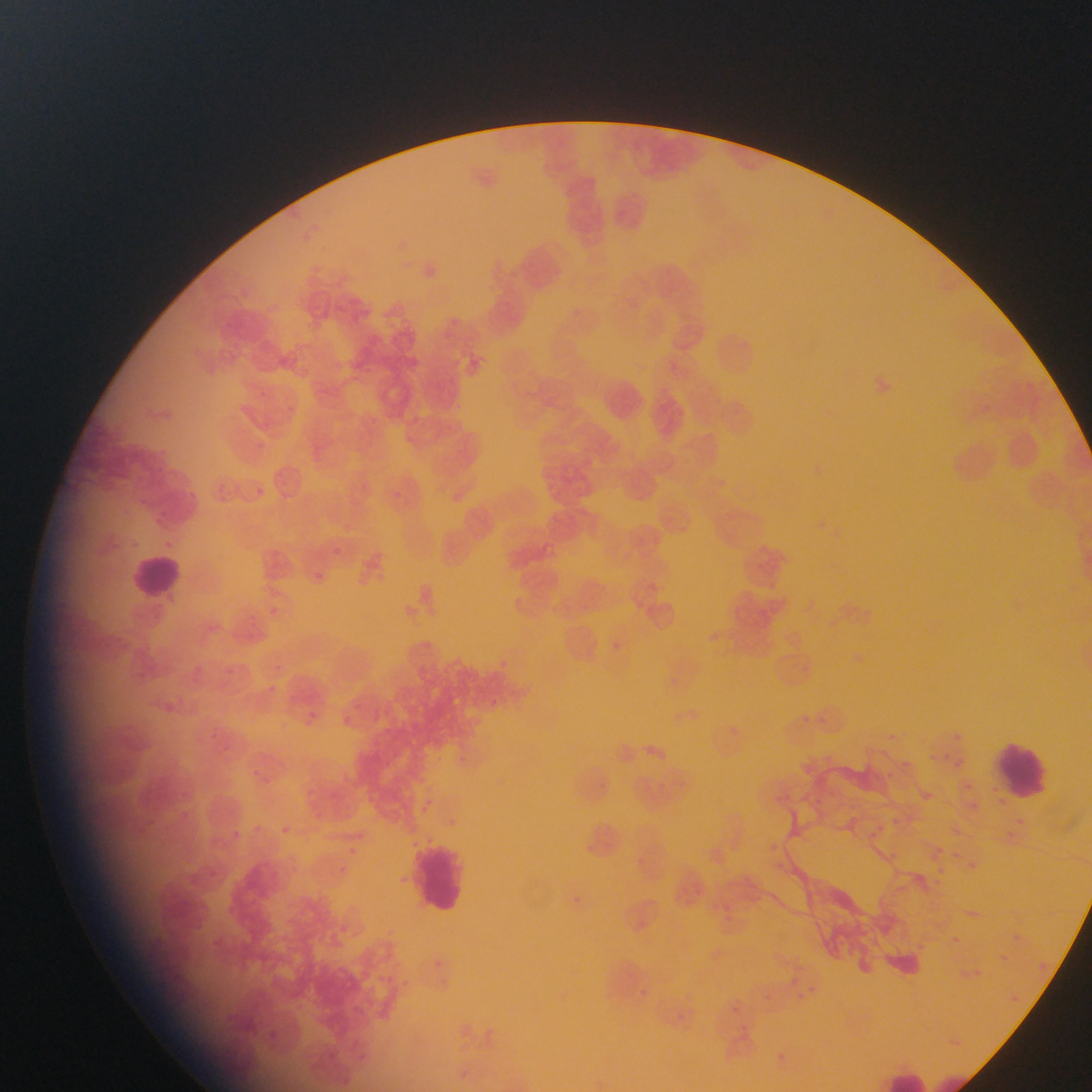
Approximate bounding boxes as (left, top, right, bottom) in pixels. Plasmodium parasite locations: (257, 488, 264, 496), (332, 546, 342, 555), (315, 571, 325, 580), (955, 732, 961, 743), (948, 751, 966, 777), (917, 789, 933, 807), (275, 824, 295, 837), (342, 842, 361, 860), (383, 868, 394, 889), (1009, 927, 1020, 940), (999, 952, 1012, 963). Leukocyte locations: (130, 549, 192, 611), (993, 739, 1053, 800), (411, 836, 468, 918), (887, 1069, 933, 1092). Image is 1092×1092 pixels. Mobile-phone photograph taken through the microscope. Thin blood smear. Collected in Ghana. Single field of view.